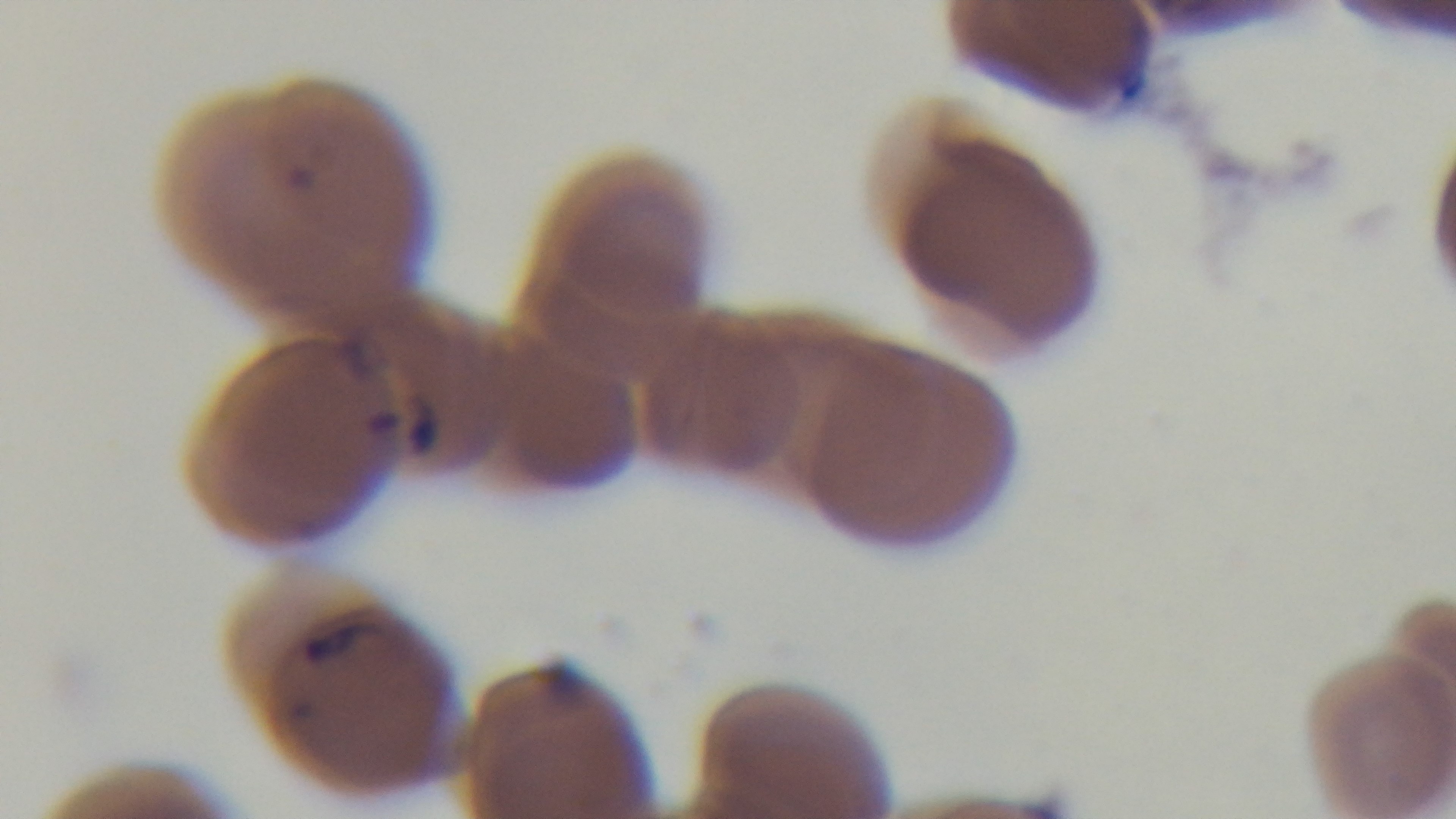
objective = 100x oil immersion
modality = light microscopy
stain = Giemsa
preparation = thin
field of view = one from the slide
malaria status = positive
capture = mounted 4K digital camera